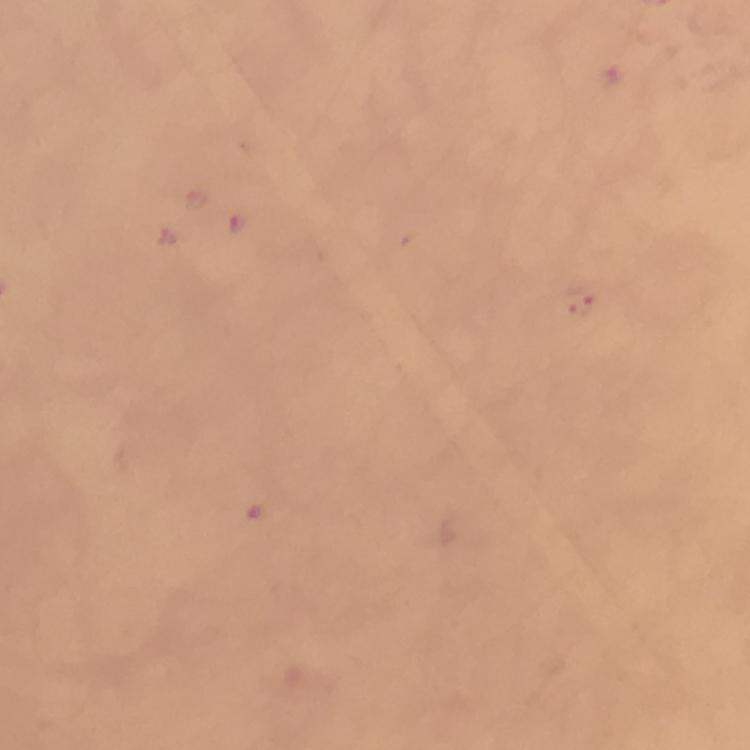
Approximate centers as {x, y} in pixels.
Summary:
  - Plasmodium parasite locations: {241, 222}, {167, 236}, {580, 302}
  - Cropped from: one field of view
  - Context: from a malaria diagnostic workup
  - Image size: 750×750 pixels
  - Magnification: 100x
  - Stain: Giemsa
  - Preparation: thick blood smear
  - Immersion oil: applied
  - Capture: smartphone photograph through a microscope